State which parasite is depicted.
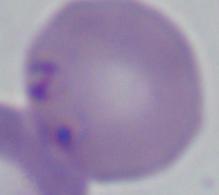

Babesia.

magnification: 1000x
modality: micrograph